Name the parasite shown.
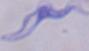

This is a trypanosome.

modality: micrograph
magnification: 1000x